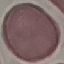

Summary:
  - Malaria status: uninfected
  - Stain: Giemsa
  - Capture: smartphone camera at the microscope eyepiece
  - Image type: cell patch, automatically extracted from a larger field of view and resized to 64 × 64 pixels
  - Preparation: thin blood film